Comment on the morphology of the red blood cells.
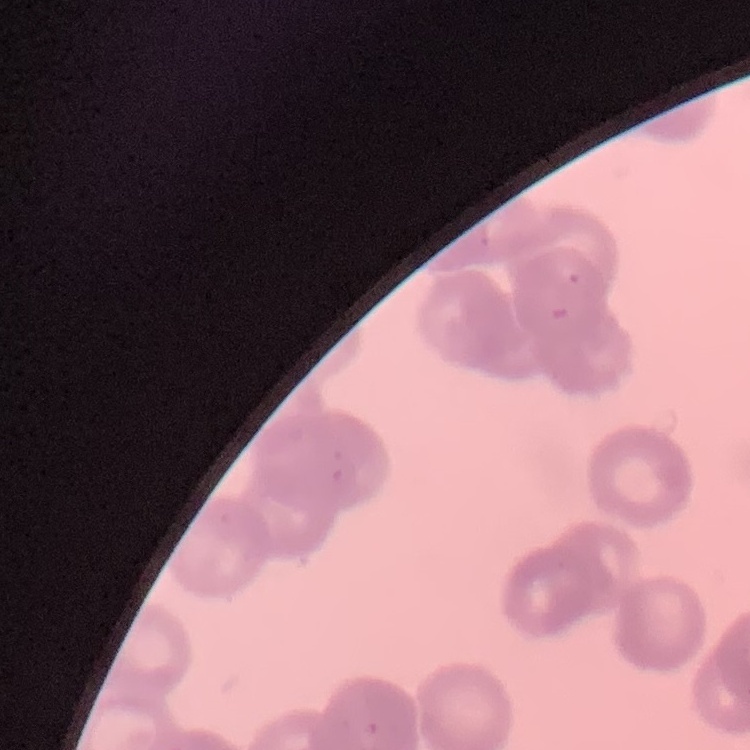
They show rouleaux formation.

image type = square crop of a larger photomicrograph
stain = Field's or Giemsa
preparation = thin peripheral smear